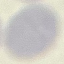

malaria status = uninfected
preparation = thin smear
stain = Giemsa
image type = cell patch, automatically extracted from a larger field of view and resized to 64 × 64 pixels
capture = smartphone through the microscope eyepiece